Locate every Plasmodium parasite and every leukocyte.
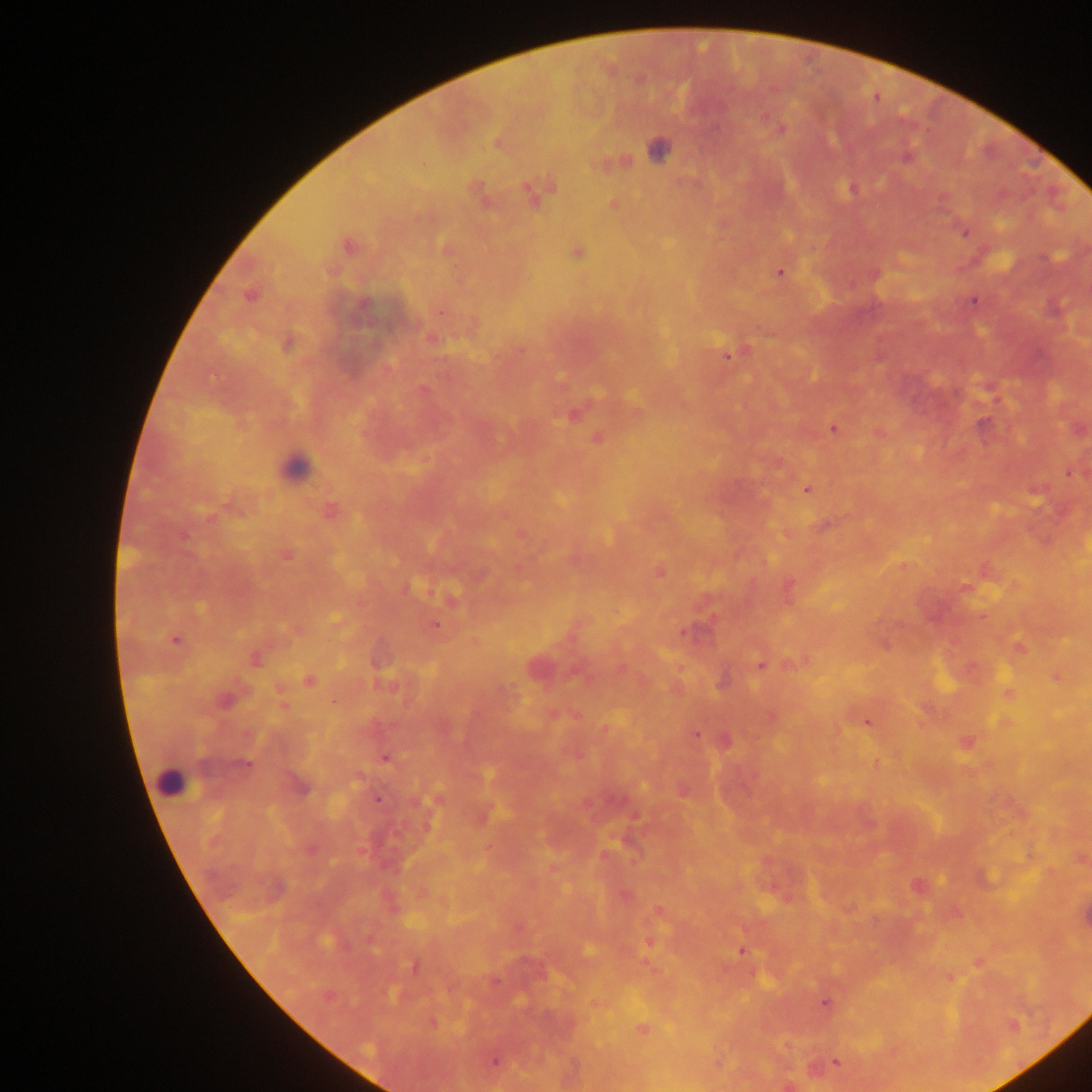
Approximate centers as {x, y} in pixels.
Plasmodium parasites: {781, 129}, {497, 143}, {907, 157}, {853, 189}, {532, 195}, {612, 204}, {965, 233}, {348, 247}, {577, 253}, {779, 272}, {249, 296}, {973, 301}, {431, 339}, {286, 344}, {727, 356}, {423, 389}, {573, 415}, {982, 424}, {833, 429}, {598, 439}, {1069, 472}, {806, 490}, {330, 511}, {184, 536}, {286, 555}, {660, 572}, {966, 588}, {435, 625}, {686, 632}, {175, 640}, {255, 660}, {760, 665}, {1056, 677}, {309, 681}, {722, 683}, {224, 701}, {867, 723}, {696, 734}, {386, 758}, {243, 765}, {377, 800}, {917, 885}, {624, 895}, {658, 912}, {651, 941}, {588, 950}, {742, 951}, {413, 966}, {825, 1003}, {433, 1023}, {1014, 1025}, {642, 1029}, {494, 1062}, {836, 1063}.
Leukocytes: {658, 150}, {295, 466}, {171, 779}.

Summary:
  - Field of view: single
  - Country: Ghana
  - Preparation: thick blood film
  - Image size: 1092×1092 pixels
  - Capture: mobile-phone photograph through a microscope